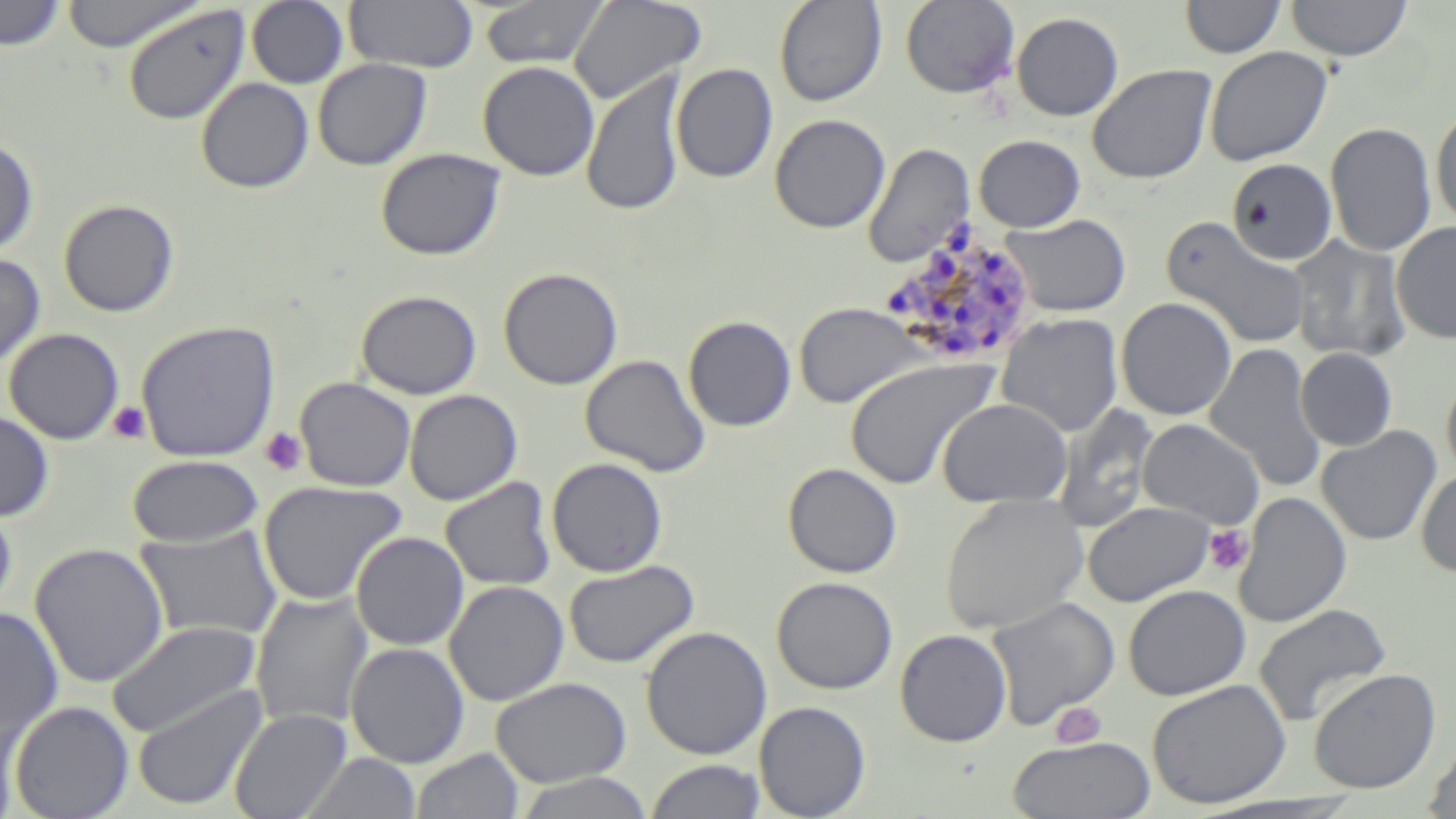
Summary:
  - Coordinate format: approximate bounding boxes as (x1,y1)-(x2,y2) corner pairs in pixels
  - Platelet locations: (108,401)-(151,443), (259,427)-(308,476), (1203,524)-(1254,575), (1049,701)-(1107,747)
  - Uninfected red blood cell locations: (0,0)-(66,51), (60,0)-(204,53), (344,0)-(478,74), (480,0)-(612,69), (568,0)-(706,105), (900,0)-(1019,98), (1180,0)-(1286,59), (1286,0)-(1413,61), (247,1)-(349,88), (775,1)-(887,107), (123,4)-(251,125), (1011,12)-(1123,121), (1204,46)-(1333,167), (312,59)-(432,171), (478,61)-(599,181), (671,63)-(778,184), (1086,64)-(1216,184), (582,71)-(687,217), (196,76)-(314,194), (1431,107)-(1456,230), (769,114)-(890,233), (1326,122)-(1437,256), (974,134)-(1086,232), (0,139)-(38,257), (863,143)-(974,268), (375,147)-(505,261), (1226,158)-(1339,265), (58,199)-(179,317), (999,213)-(1131,317), (1162,217)-(1311,349), (1392,222)-(1456,343), (1289,235)-(1410,363), (0,252)-(46,370), (498,267)-(623,390), (356,290)-(481,400), (1116,297)-(1237,421), (794,301)-(926,408), (996,313)-(1123,438), (683,315)-(797,432), (135,320)-(279,462), (4,328)-(124,445), (1205,342)-(1325,491), (1296,348)-(1397,451), (580,354)-(711,476), (845,356)-(998,490), (1441,376)-(1456,483), (295,377)-(416,491), (404,389)-(522,505), (937,397)-(1072,507), (1051,402)-(1160,534), (0,409)-(54,522), (1136,418)-(1265,529), (1316,425)-(1441,546), (127,454)-(264,547), (547,457)-(668,577), (783,463)-(902,578), (1416,469)-(1456,578), (440,477)-(557,592), (258,479)-(407,606), (1234,491)-(1351,628), (939,494)-(1091,635), (0,501)-(17,617), (1083,501)-(1215,606), (135,526)-(283,643), (351,531)-(469,651), (30,541)-(170,688), (563,559)-(699,669), (772,576)-(897,694), (444,580)-(568,706), (1123,584)-(1250,700), (250,591)-(373,730), (985,596)-(1120,730), (1253,603)-(1392,728), (0,607)-(64,742), (104,620)-(262,739), (641,626)-(772,760), (895,629)-(1012,746), (345,642)-(470,768), (1308,667)-(1441,794), (491,677)-(631,787), (1146,679)-(1291,809), (131,683)-(267,811), (9,700)-(133,818), (754,701)-(871,818), (0,706)-(25,818), (229,708)-(352,819), (1007,735)-(1157,818), (1424,738)-(1456,819), (410,748)-(525,819), (300,752)-(421,818), (644,760)-(766,818), (511,772)-(656,819)
  - Plasmodium malariae-infected red blood cell locations: (877,232)-(1038,367)
  - Slide-level diagnosis: Plasmodium malariae
  - Preparation: thin blood smear
  - Image size: 1456×819 pixels
  - Modality: light microscopy
  - Stain: May-Grünwald-Giemsa
  - Field of view: single
  - Magnification: 1000x